Give the extent of all uninfected red blood cells.
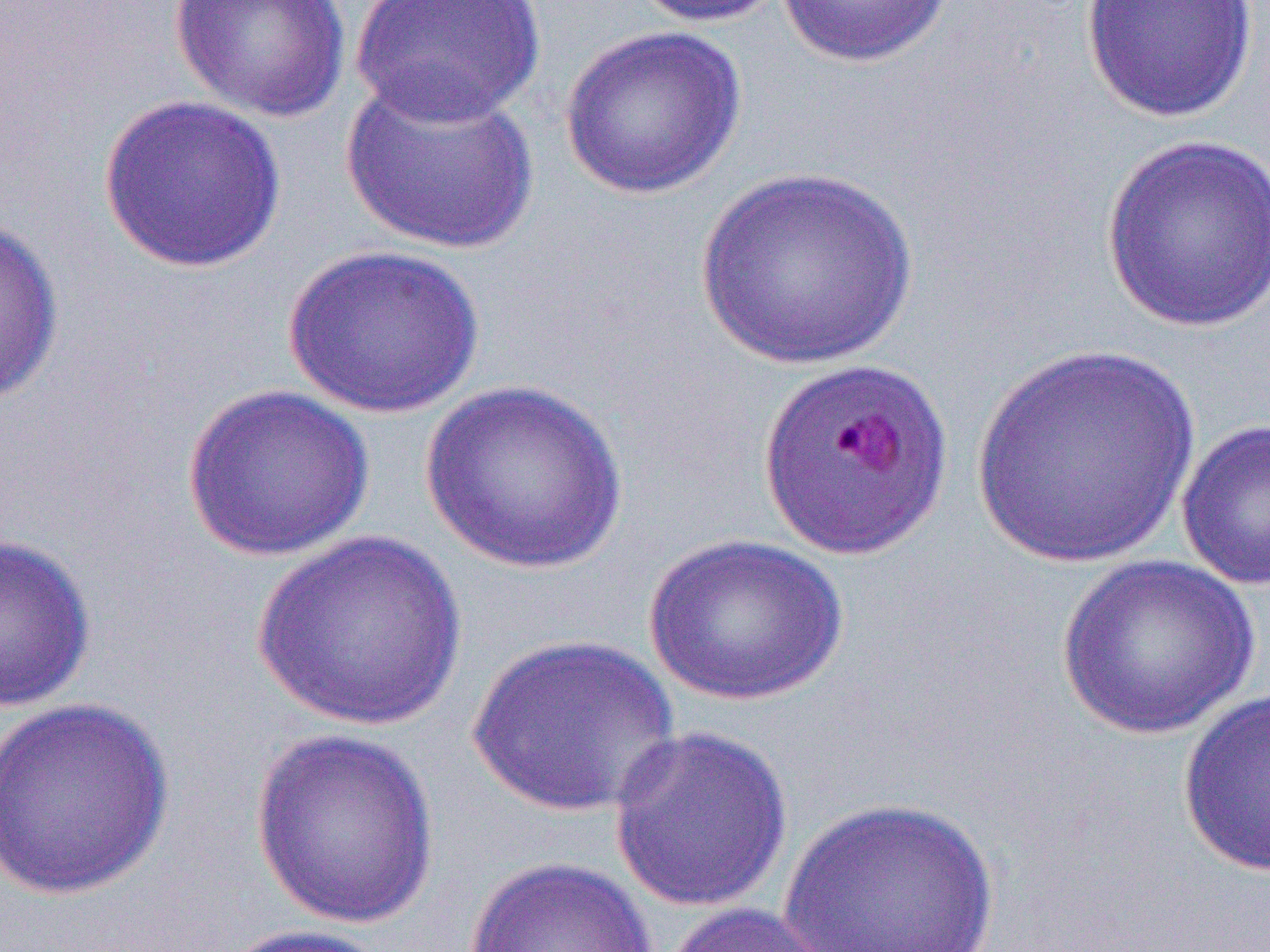

Approximate bounding boxes as (x1,y1)-(x2,y2) corner pairs in pixels.
Uninfected red blood cells: (168,0)-(353,123), (348,0)-(547,126), (626,0)-(791,28), (774,0)-(959,69), (1079,0)-(1260,124), (558,24)-(748,201), (340,70)-(538,254), (97,94)-(288,274), (1100,134)-(1270,334), (696,166)-(918,370), (0,215)-(65,405), (283,245)-(485,418), (967,345)-(1202,572), (418,379)-(630,574), (181,383)-(375,561), (1176,418)-(1270,592), (252,529)-(466,732), (0,532)-(97,713), (643,532)-(849,706), (1056,554)-(1260,740), (466,633)-(681,819), (1178,688)-(1270,879), (0,697)-(176,900), (607,724)-(794,914), (249,728)-(441,930), (778,796)-(1002,952), (464,855)-(660,952), (658,901)-(848,952), (214,923)-(395,952).

Slide-level diagnosis: Plasmodium falciparum. Light microscopy. Thin blood smear. Single field of view. 1000x magnification. Image is 1270×952 pixels.